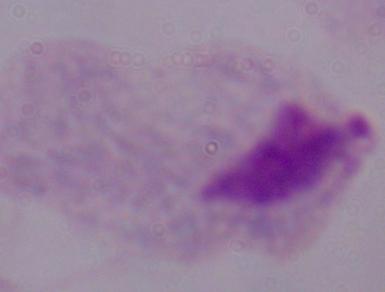
1000x magnification. Photomicrograph. A trichomonad is shown.